Describe the morphology of the erythrocytes.
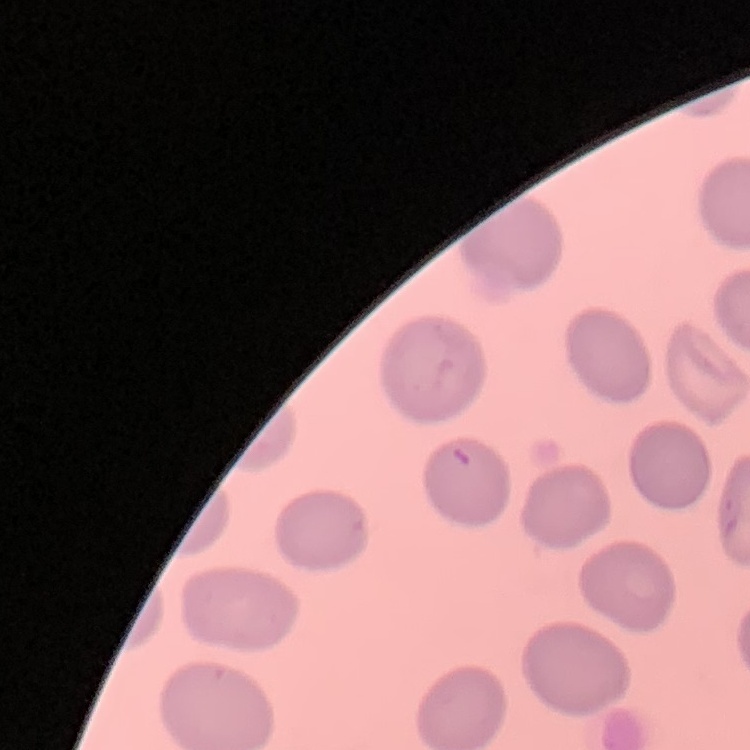
No rouleaux formation.

Summary:
  - Preparation: thin peripheral smear
  - Image type: square crop of a larger photomicrograph
  - Stain: Field's or Giemsa